Name the cell type shown.
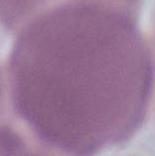
This is an erythrocyte.

magnification = 1000x
modality = photomicrograph